State which cell type is depicted.
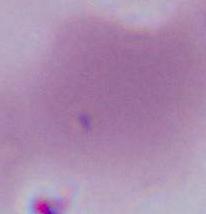
An erythrocyte.

modality = photomicrograph
magnification = 1000x